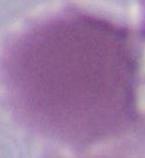

Micrograph. 1000x magnification. An erythrocyte is shown.